Comment on the morphology of the red blood cells.
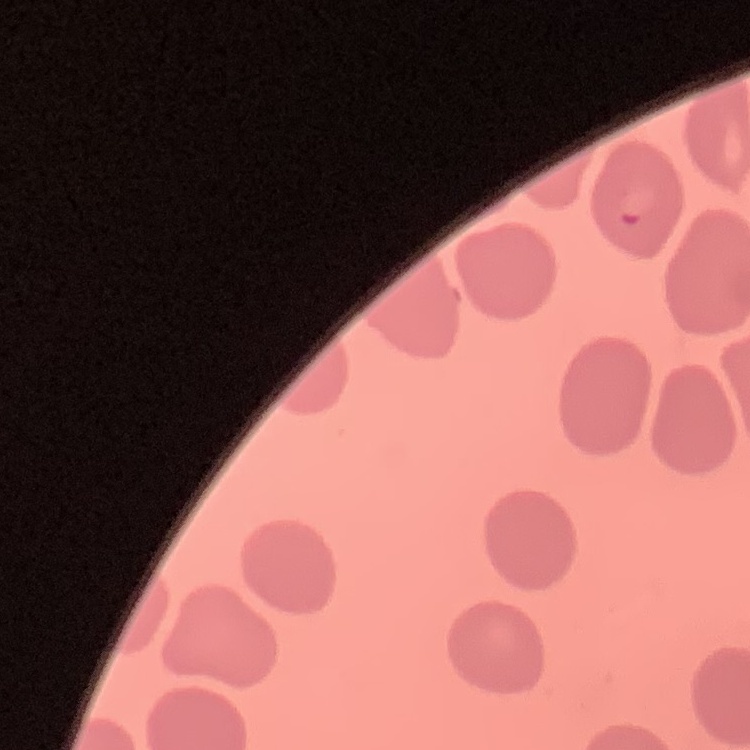
They show no rouleaux formation.

Summary:
  - Image type: square crop of a larger photomicrograph
  - Preparation: thin blood film
  - Stain: Field's or Giemsa